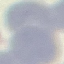

Summary:
  - Result: negative for malaria parasites
  - Preparation: thin blood smear
  - Image type: automatically extracted cell patch, resized to 64 × 64 pixels
  - Capture: smartphone camera at the microscope eyepiece
  - Stain: Giemsa